State which parasite is depicted.
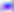

Toxoplasma gondii.

400x magnification. Photomicrograph.